Assess this cell for malaria.
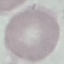

It is uninfected.

image type = cell patch, automatically extracted from a larger field of view and resized to 64 × 64 pixels
capture = smartphone through the microscope eyepiece
stain = Giemsa
preparation = thin blood film